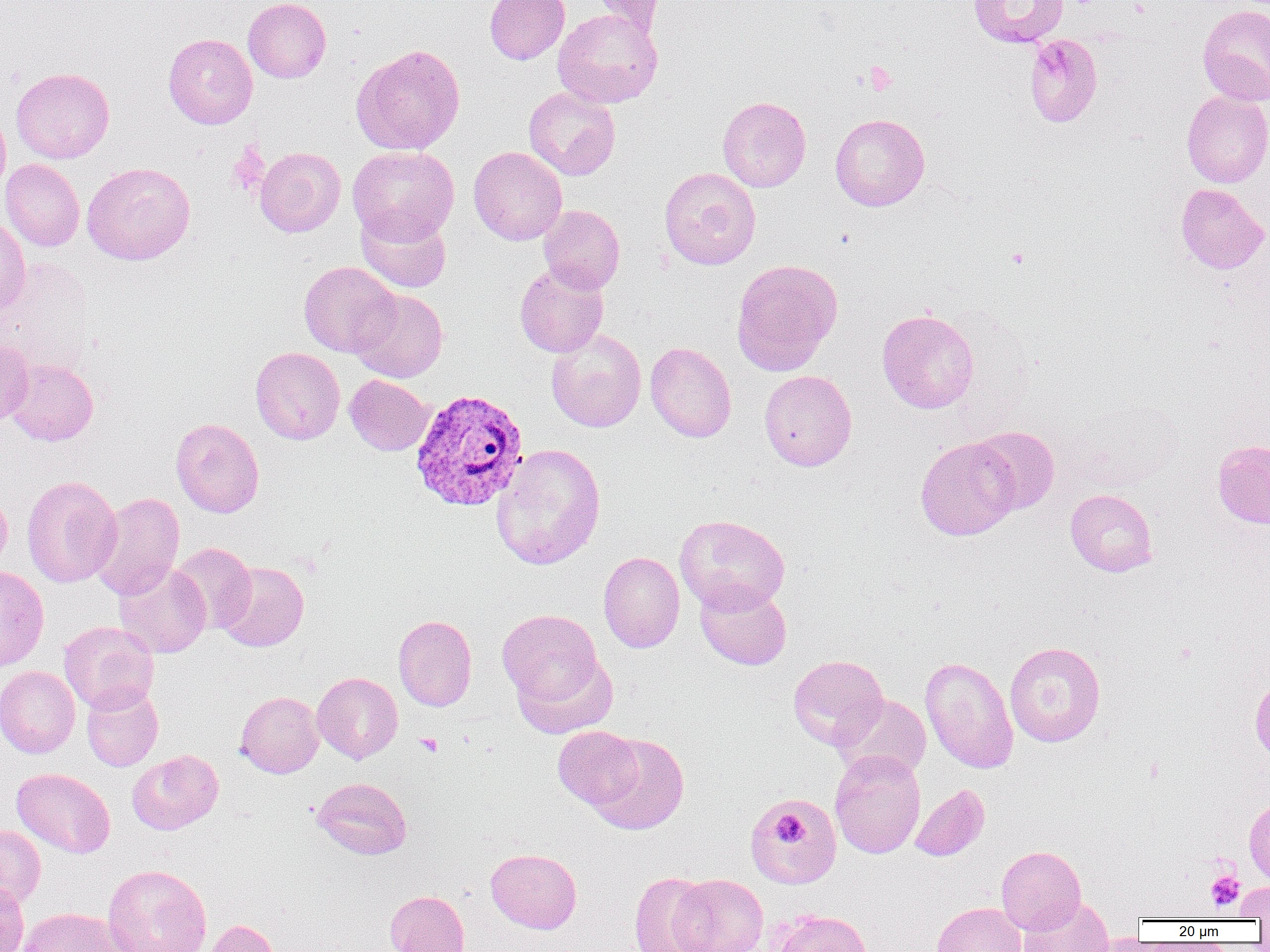

slide_level_diagnosis: Plasmodium vivax
platelet_locations: 'approximate bounding boxes as [x1, y1, x2, y2] in pixels: [862, 61, 897, 95], [1006, 247, 1029, 269], [416, 733, 442, 756], [772, 814, 805, 845], [1206, 871, 1245, 912]'
uninfected_red_blood_cell_locations: 'approximate bounding boxes as [x1, y1, x2, y2] in pixels: [243, 0, 331, 83], [484, 0, 570, 64], [590, 0, 666, 36], [967, 0, 1069, 48], [1197, 3, 1270, 106], [553, 9, 663, 108], [163, 33, 257, 129], [1024, 33, 1103, 128], [352, 44, 466, 155], [11, 67, 114, 164], [523, 87, 621, 180], [1181, 91, 1270, 187], [717, 95, 811, 192], [0, 105, 11, 198], [830, 113, 930, 211], [254, 146, 346, 237], [347, 146, 459, 245], [469, 146, 567, 245], [0, 159, 85, 251], [82, 162, 195, 265], [659, 167, 761, 270], [1175, 183, 1268, 274], [539, 204, 625, 294], [355, 208, 452, 294], [0, 214, 30, 315], [731, 259, 843, 376], [298, 261, 400, 357], [514, 263, 609, 358], [349, 288, 448, 382], [877, 308, 979, 414], [546, 329, 646, 432], [0, 339, 34, 427], [645, 342, 736, 442], [251, 346, 345, 444], [5, 358, 98, 446], [759, 369, 857, 471], [344, 374, 434, 456], [1064, 399, 1185, 493], [171, 417, 264, 518], [969, 425, 1060, 515], [915, 437, 1019, 541], [1212, 439, 1270, 528], [491, 444, 606, 571], [21, 475, 122, 588], [1065, 488, 1158, 577], [0, 490, 11, 574], [89, 492, 184, 600], [675, 514, 790, 614], [169, 542, 256, 634], [598, 551, 685, 653], [217, 561, 309, 652], [114, 562, 211, 658], [0, 566, 49, 671], [695, 581, 792, 670], [497, 608, 606, 716], [393, 614, 477, 711], [59, 621, 159, 714], [1004, 641, 1106, 747], [788, 654, 888, 750], [920, 656, 1018, 774], [0, 665, 80, 758], [312, 672, 403, 763], [1250, 674, 1270, 764], [81, 686, 163, 771], [235, 691, 324, 778], [833, 693, 932, 781], [553, 725, 644, 810], [588, 732, 690, 835], [127, 750, 223, 835], [830, 750, 925, 859], [12, 767, 115, 858], [312, 777, 412, 859], [910, 783, 990, 861], [750, 794, 841, 887], [1244, 798, 1270, 886], [0, 825, 45, 907], [996, 845, 1086, 934], [485, 848, 582, 933], [102, 864, 212, 952], [628, 872, 716, 951], [670, 874, 768, 952], [0, 880, 29, 952], [1234, 881, 1270, 920], [385, 889, 469, 952], [1018, 897, 1114, 952], [931, 901, 1027, 952], [17, 907, 131, 952], [771, 909, 872, 952], [205, 919, 280, 952]'
modality: light microscopy
plasmodium_vivax_infected_red_blood_cell_locations: 'approximate bounding boxes as [x1, y1, x2, y2] in pixels: [409, 388, 529, 513]'
image_size: 1270×952 pixels
magnification: 1000x
preparation: thin blood smear
field_of_view: one of a larger specimen